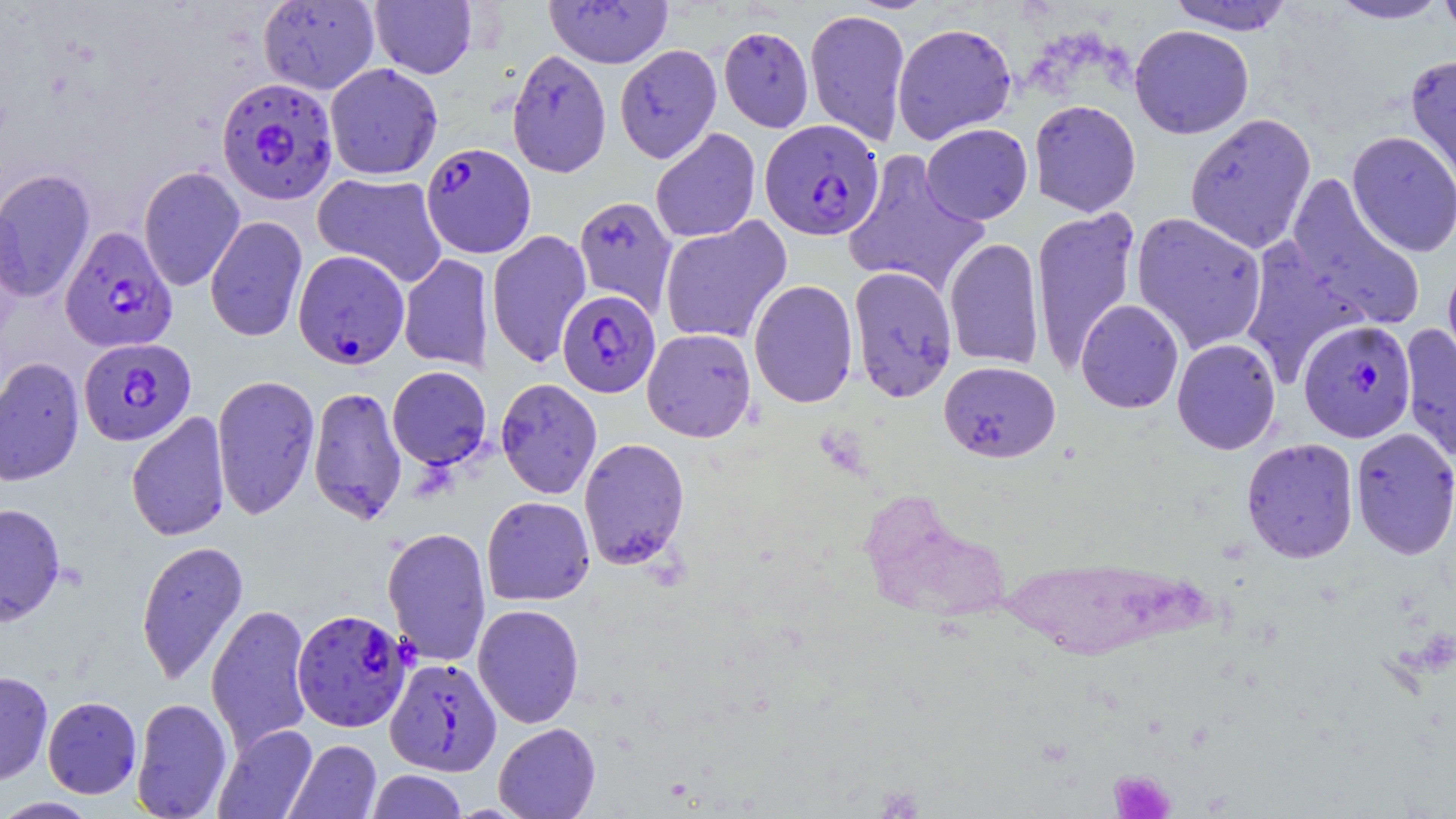 Approximate bounding boxes as (x1, y1, x2, y2) in pixels. Plasmodium falciparum-infected red blood cell locations: (216, 77, 339, 206), (759, 119, 884, 241), (421, 142, 536, 258), (59, 226, 177, 353), (292, 249, 410, 369), (557, 290, 661, 397), (1298, 319, 1417, 443), (78, 338, 196, 446), (292, 608, 412, 731), (385, 657, 502, 776). Uninfected red blood cell locations: (545, 0, 673, 69), (1327, 0, 1450, 24), (1438, 0, 1456, 43), (258, 1, 380, 94), (369, 1, 477, 79), (1165, 1, 1297, 35), (804, 9, 911, 147), (891, 23, 1017, 144), (1129, 24, 1254, 139), (718, 25, 814, 132), (614, 44, 722, 163), (506, 48, 611, 177), (1404, 54, 1456, 199), (324, 62, 443, 180), (1028, 99, 1141, 217), (1184, 113, 1316, 254), (921, 123, 1033, 225), (650, 128, 761, 243), (1346, 130, 1456, 257), (842, 150, 990, 297), (138, 165, 246, 292), (0, 168, 96, 301), (312, 172, 448, 288), (1285, 175, 1426, 330), (573, 195, 677, 315), (1030, 206, 1141, 375), (1131, 212, 1268, 354), (205, 215, 308, 342), (659, 216, 792, 345), (486, 229, 592, 369), (944, 237, 1045, 370), (1239, 237, 1367, 384), (398, 253, 493, 372), (1441, 261, 1456, 380), (848, 266, 958, 402), (748, 279, 859, 409), (1076, 299, 1184, 414), (1399, 324, 1456, 465), (642, 328, 756, 442), (1171, 338, 1281, 454), (0, 357, 84, 487), (939, 360, 1061, 462), (387, 366, 492, 470), (212, 374, 320, 520), (495, 378, 602, 499), (308, 385, 407, 526), (126, 411, 230, 542), (1349, 427, 1456, 560), (578, 437, 690, 570), (1241, 438, 1359, 563), (481, 496, 595, 606), (0, 502, 66, 628), (382, 526, 492, 667), (135, 540, 249, 686), (206, 603, 314, 754), (473, 604, 584, 728), (0, 670, 53, 787), (42, 696, 142, 799), (130, 697, 233, 819), (493, 723, 600, 819), (213, 724, 318, 819), (285, 739, 382, 819), (366, 770, 468, 818), (0, 797, 101, 818). Platelet locations: (1110, 769, 1177, 818). Slide-level diagnosis: Plasmodium falciparum. One field of a larger specimen. May-Grünwald-Giemsa stain. Optical microscopy. Captured at 1000x magnification. Image is 1456×819 pixels. Thin blood film.